Assess this cell for malaria.
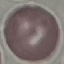

It is uninfected.

Automatically extracted cell patch, resized to 64 × 64 pixels. Thin blood smear. Acquired by smartphone through the microscope eyepiece. Giemsa-stained preparation.